Assess this cell for malaria.
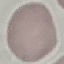
Uninfected.

preparation = thin blood film
image type = cell patch, automatically extracted from a larger field of view and resized to 64 × 64 pixels
stain = Giemsa
capture = smartphone through the microscope eyepiece